Comment on the morphology of the red blood cells.
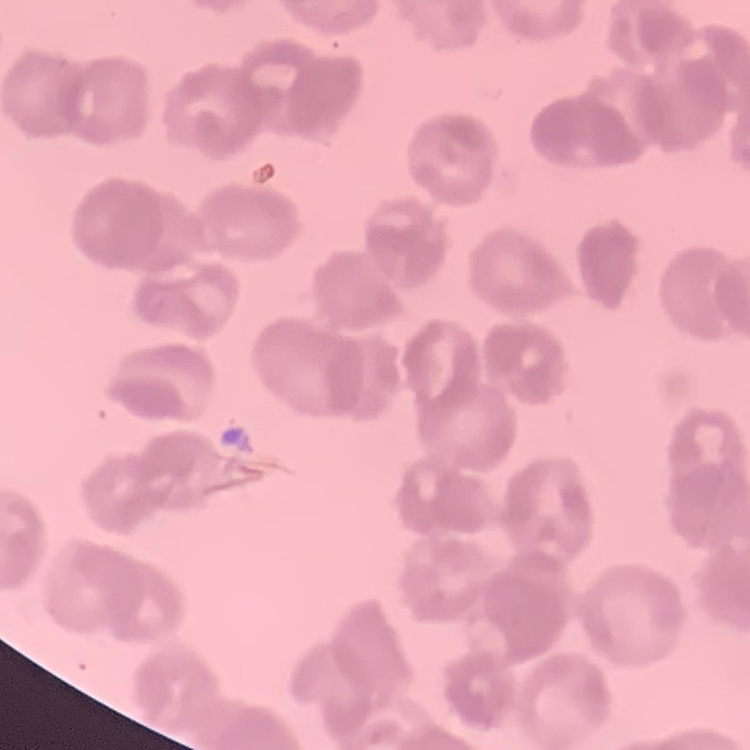

They show rouleaux formation.

Field's or Giemsa stain. Thin blood smear. One tile cut from a larger photomicrograph.